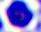
Captured at 400x magnification. Micrograph. A white blood cell is seen.